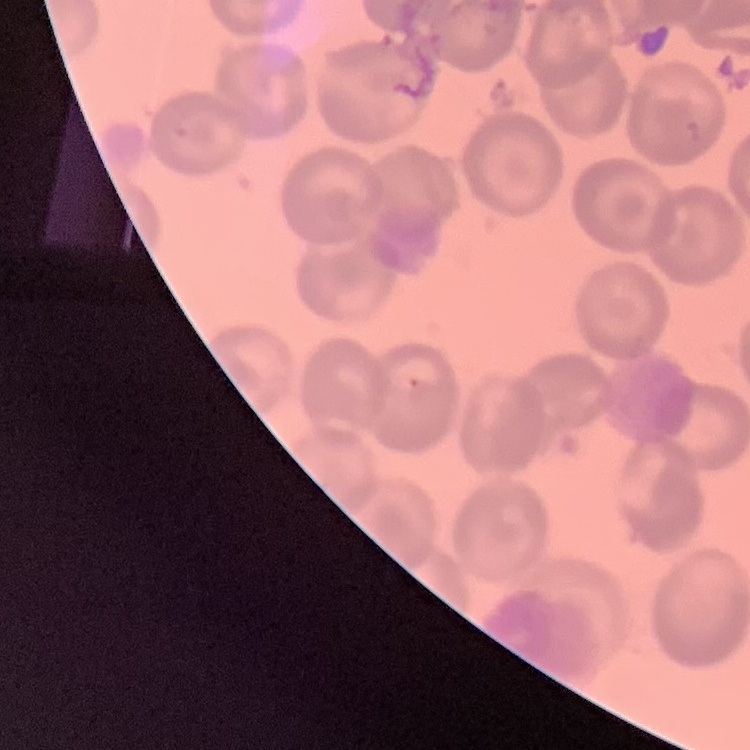
erythrocyte morphology = no rouleaux formation
preparation = thin blood film
image type = one tile cut from a larger photomicrograph
stain = Field's or Giemsa